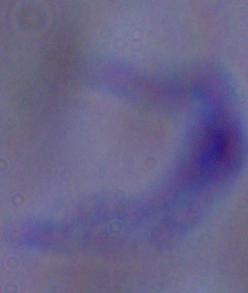
Summary:
  - Magnification: 1000x
  - Identification: trypanosome
  - Modality: photomicrograph